Point out each Plasmodium parasite.
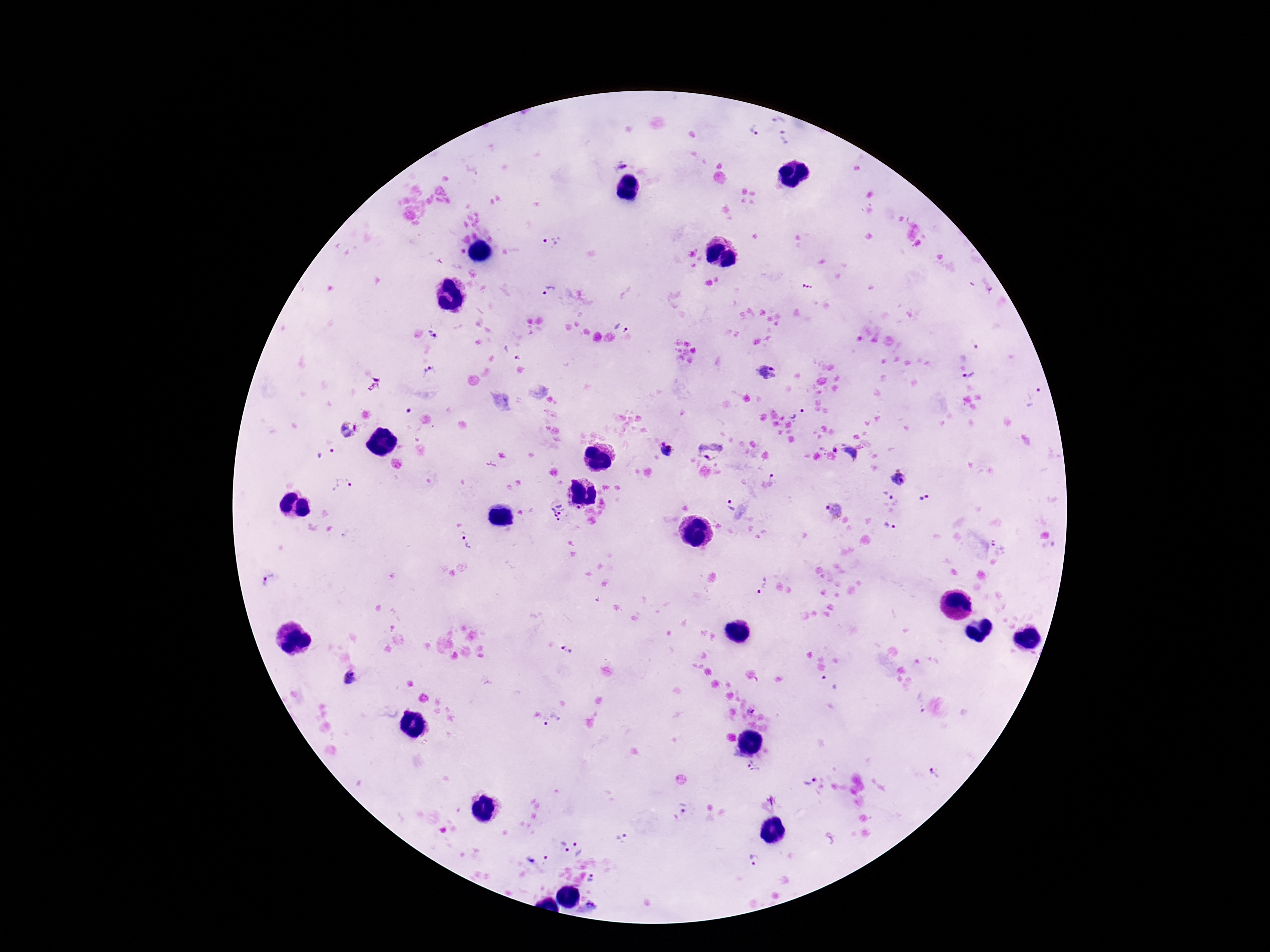

Approximate centers as {x, y} in pixels.
Plasmodium parasites: {777, 119}, {754, 131}, {786, 138}, {624, 163}, {552, 243}, {549, 289}, {623, 326}, {434, 333}, {767, 372}, {430, 373}, {970, 377}, {1033, 397}, {799, 416}, {348, 431}, {711, 447}, {667, 450}, {848, 453}, {328, 456}, {899, 478}, {773, 479}, {343, 485}, {887, 494}, {925, 497}, {730, 505}, {557, 511}, {834, 511}, {890, 527}, {467, 541}, {999, 545}, {271, 581}, {761, 585}, {566, 650}, {351, 677}, {829, 681}, {919, 703}, {752, 709}, {551, 720}, {753, 767}, {935, 773}, {810, 778}, {683, 808}, {562, 847}, {582, 847}, {753, 858}, {539, 859}, {592, 880}, {589, 908}.

Giemsa-stained preparation. Photographed through the microscope eyepiece with a smartphone camera. Single field of view. 100x magnification. Thick blood film. Image is 1270×952 pixels. Patient malaria status: positive.